Assess this cell for malaria.
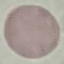

It is uninfected.

Photographed with a smartphone camera at the microscope eyepiece. Thin blood smear. Automatically extracted cell patch, resized to 64 × 64 pixels. Giemsa stain.